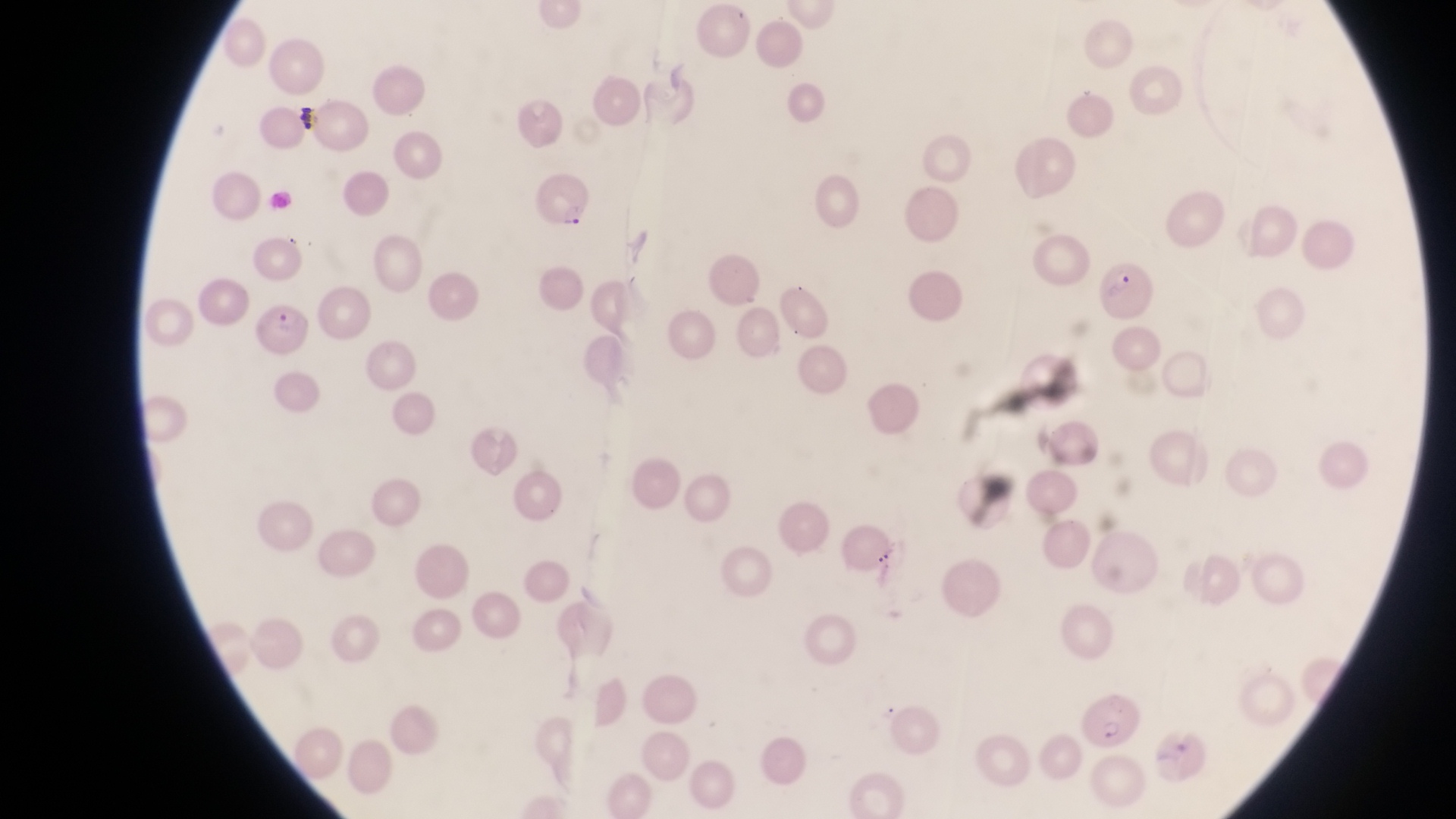

artifact (platelet-like body, stain precipitate, or debris) locations = approximate bounding boxes as {left, top, right, bottom} in pixels: {296, 105, 317, 138}
capture = smartphone photograph through the eyepiece of an Olympus CX-23 microscope
parasitised red blood cell locations = approximate bounding boxes as {left, top, right, bottom} in pixels: {536, 168, 589, 232}, {1105, 259, 1154, 318}, {256, 301, 308, 356}, {1078, 693, 1141, 748}
preparation = thin blood smear
country = Uganda
field of view = single
magnification = 1000x
image size = 1456×819 pixels